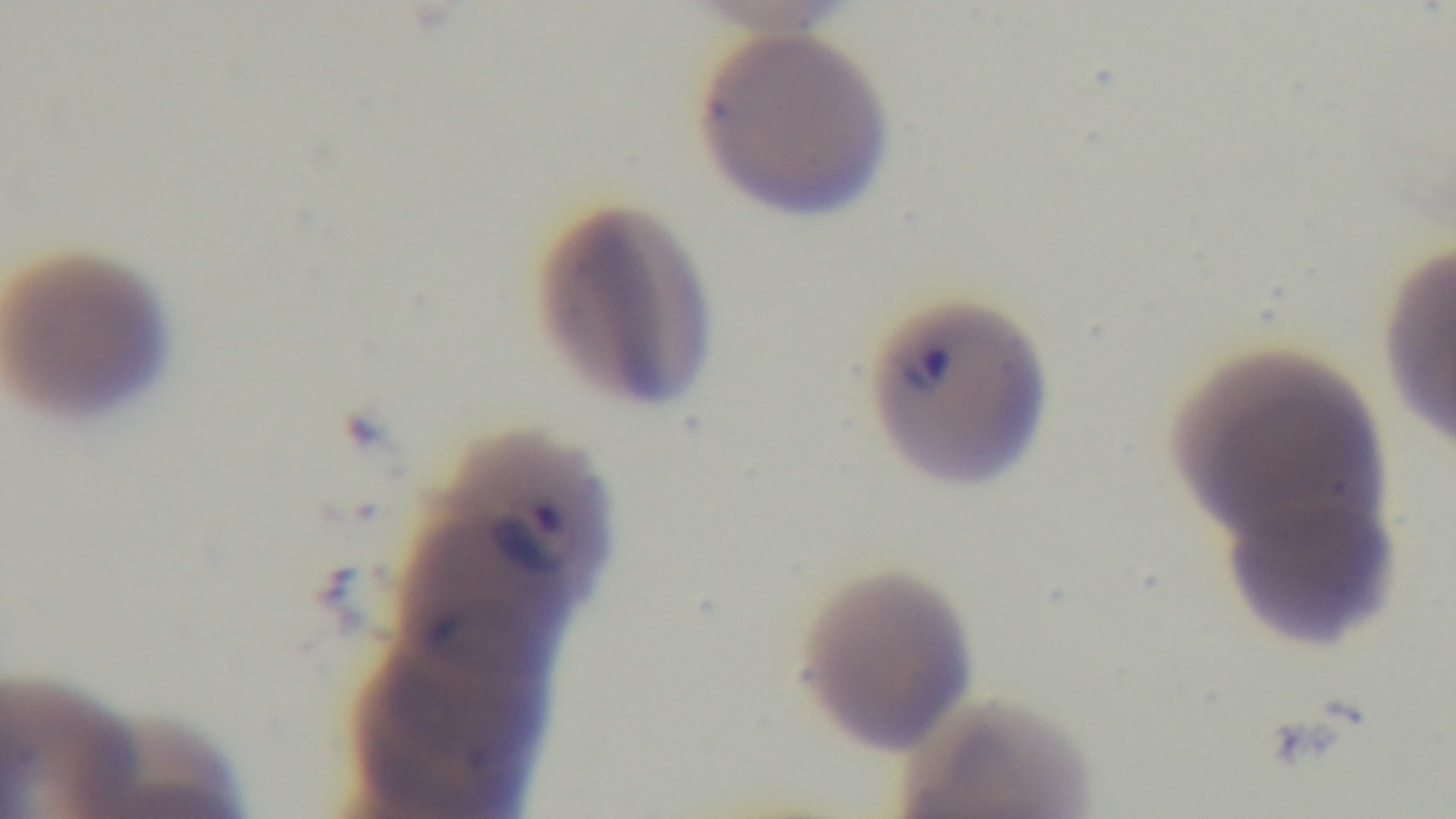

{
  "objective": "100x oil immersion",
  "capture": "mounted 4K digital camera",
  "malaria_status": "positive",
  "preparation": "thin smear",
  "stain": "Giemsa",
  "field_of_view": "single",
  "modality": "light microscopy"
}